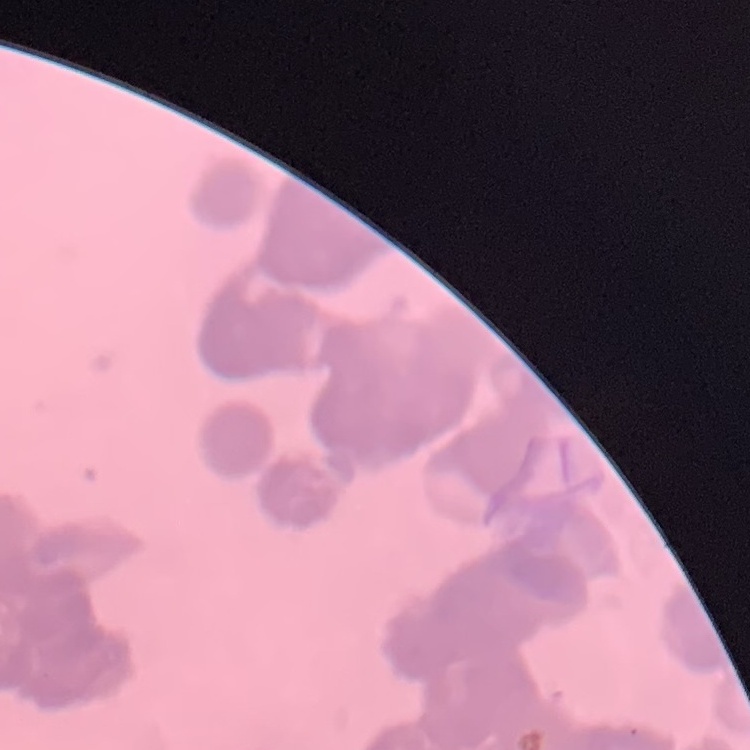
Summary:
  - Erythrocyte morphology: rouleaux formation
  - Preparation: thin blood smear
  - Stain: Field's or Giemsa
  - Image type: square crop of a larger photomicrograph